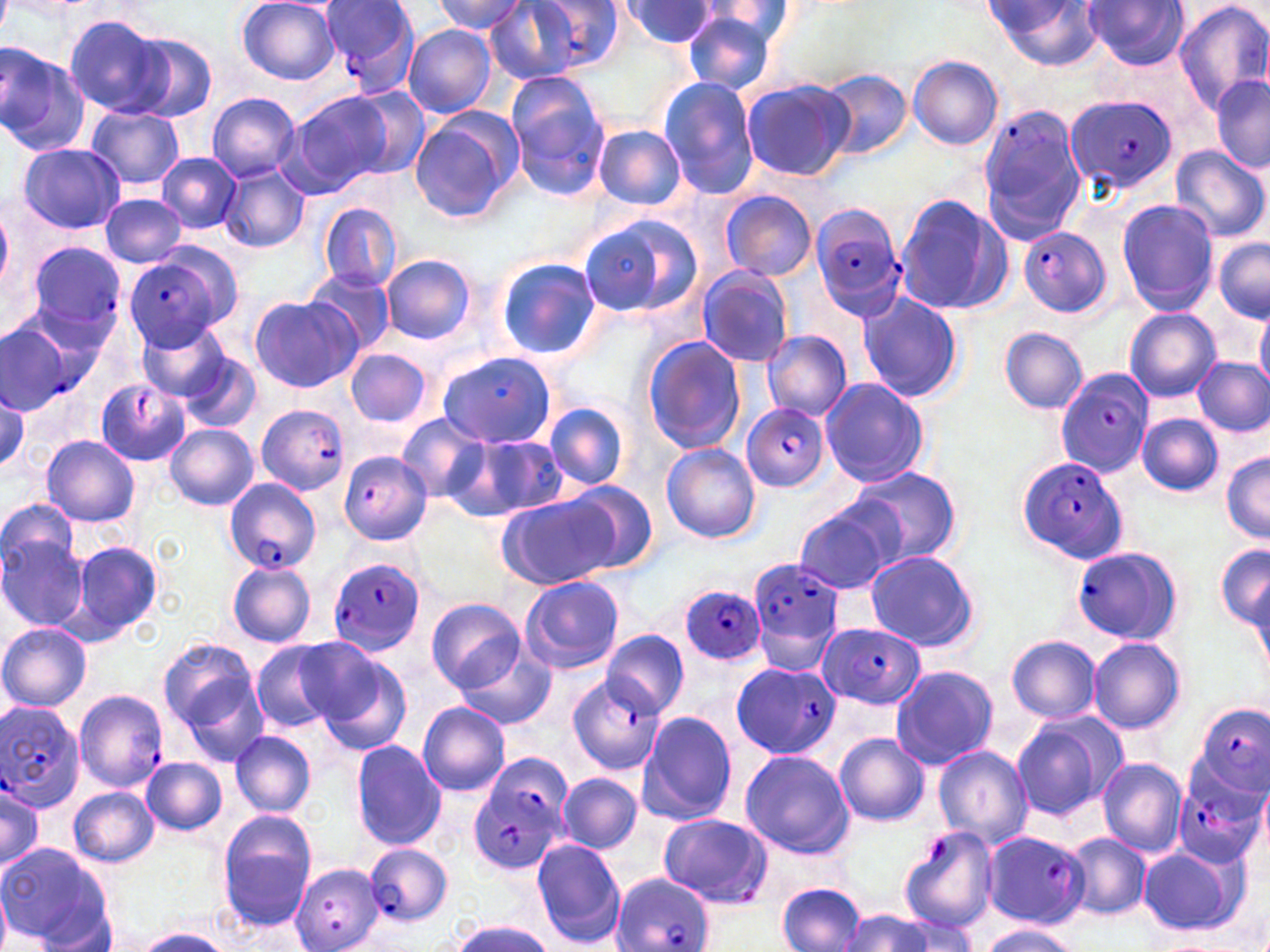

Summary:
  - Coordinate format: approximate bounding boxes as (x1, y1, x2, y2) in pixels
  - Plasmodium falciparum-infected red blood cell locations (subset): (524, 0, 625, 73), (321, 1, 418, 98), (1064, 96, 1175, 193), (979, 108, 1087, 206), (811, 203, 908, 321), (1021, 226, 1110, 317), (26, 242, 126, 337), (128, 247, 242, 348), (1056, 367, 1154, 475), (96, 379, 191, 467), (742, 403, 828, 493), (257, 404, 350, 496), (1016, 456, 1128, 565), (225, 478, 320, 573), (1072, 546, 1182, 643), (328, 559, 425, 656), (748, 559, 846, 669), (680, 583, 768, 666), (816, 627, 922, 708), (731, 661, 841, 759), (568, 674, 665, 776), (74, 690, 169, 793), (0, 703, 83, 814), (1195, 703, 1270, 797), (1174, 758, 1269, 870), (466, 766, 569, 876), (659, 813, 772, 907), (982, 829, 1089, 929), (363, 843, 451, 926), (288, 863, 385, 951), (610, 872, 714, 952)
  - Uninfected red blood cell locations (subset): (1084, 0, 1190, 70), (1173, 0, 1270, 114), (237, 1, 340, 85), (435, 1, 530, 34), (623, 1, 722, 48), (987, 1, 1105, 71), (486, 2, 589, 83), (694, 2, 795, 51), (681, 10, 779, 98), (64, 15, 171, 117), (404, 26, 495, 117), (126, 33, 217, 121), (0, 41, 87, 155), (908, 56, 1003, 150), (821, 69, 912, 161), (1212, 74, 1270, 171), (740, 77, 856, 182), (506, 78, 610, 200), (659, 78, 762, 198), (344, 86, 430, 182), (285, 92, 390, 195), (208, 93, 302, 180), (87, 104, 185, 191), (410, 112, 519, 224), (594, 125, 688, 209), (17, 143, 125, 234), (1170, 144, 1269, 243), (157, 152, 241, 233), (218, 163, 309, 254), (720, 190, 818, 281), (99, 193, 187, 267), (896, 193, 1015, 316), (1117, 199, 1218, 315), (319, 202, 402, 291), (0, 205, 13, 299), (578, 213, 703, 320), (1213, 238, 1270, 321), (383, 254, 475, 342), (496, 258, 601, 359), (303, 267, 395, 354), (698, 268, 794, 368), (859, 293, 963, 404), (251, 296, 359, 391), (7, 298, 109, 396), (1254, 307, 1270, 395), (1124, 308, 1221, 402), (139, 321, 231, 401), (0, 322, 72, 412), (999, 327, 1087, 414), (761, 330, 852, 421), (643, 337, 746, 454), (346, 348, 431, 427), (180, 350, 260, 433), (1194, 357, 1270, 436), (821, 378, 928, 488), (0, 392, 26, 475), (546, 403, 628, 489), (1137, 413, 1223, 495), (397, 414, 487, 503), (165, 423, 258, 510), (41, 436, 139, 526), (466, 436, 570, 520), (661, 443, 759, 543), (1220, 453, 1270, 543), (848, 467, 957, 566), (566, 480, 659, 575), (498, 496, 614, 590), (793, 500, 902, 596), (0, 524, 90, 632), (66, 540, 164, 643), (1215, 542, 1269, 630), (863, 550, 980, 650), (228, 562, 316, 646), (521, 575, 625, 674), (1249, 578, 1270, 688), (427, 598, 525, 692), (0, 623, 91, 710), (602, 631, 688, 717), (1006, 635, 1102, 723), (1087, 636, 1186, 735), (159, 638, 258, 731), (253, 642, 338, 734), (455, 646, 556, 730), (312, 648, 412, 755), (889, 664, 998, 771), (179, 677, 270, 769), (418, 702, 510, 796), (636, 710, 737, 826), (1010, 711, 1127, 824), (231, 730, 316, 817), (834, 732, 928, 826), (351, 741, 447, 849), (933, 745, 1034, 848), (740, 750, 855, 860), (141, 757, 227, 835), (1097, 757, 1188, 858), (558, 773, 642, 854), (0, 780, 44, 872), (69, 787, 159, 867), (217, 811, 318, 931), (1064, 833, 1151, 921), (531, 837, 627, 948), (0, 842, 113, 950), (1137, 845, 1246, 937), (0, 882, 13, 952), (777, 882, 866, 951), (838, 910, 933, 952), (882, 912, 980, 952), (446, 920, 557, 952), (977, 925, 1083, 952), (135, 928, 232, 952)
  - Slide-level diagnosis: Plasmodium falciparum
  - Magnification: 1000x
  - Stain: May-Grünwald-Giemsa
  - Field of view: one of a larger specimen
  - Modality: optical microscopy
  - Image size: 1270×952 pixels
  - Preparation: thin blood smear